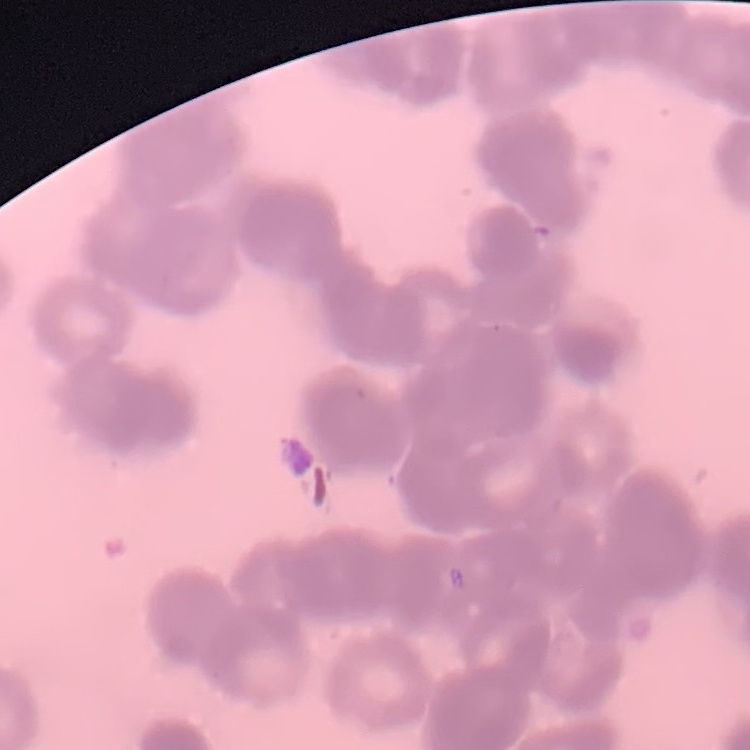
{
  "erythrocyte_morphology": "rouleaux formation",
  "preparation": "thin blood film",
  "stain": "Field's or Giemsa",
  "image_type": "square crop of a larger photomicrograph"
}